Comment on the morphology of the erythrocytes.
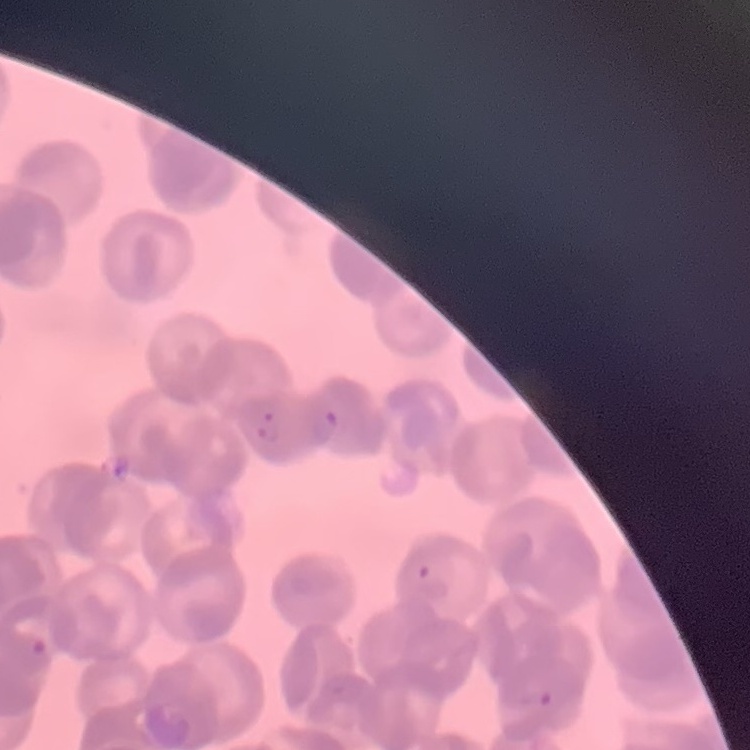

They show rouleaux formation.

preparation = thin blood film
image type = square crop of a larger photomicrograph
stain = Field's or Giemsa